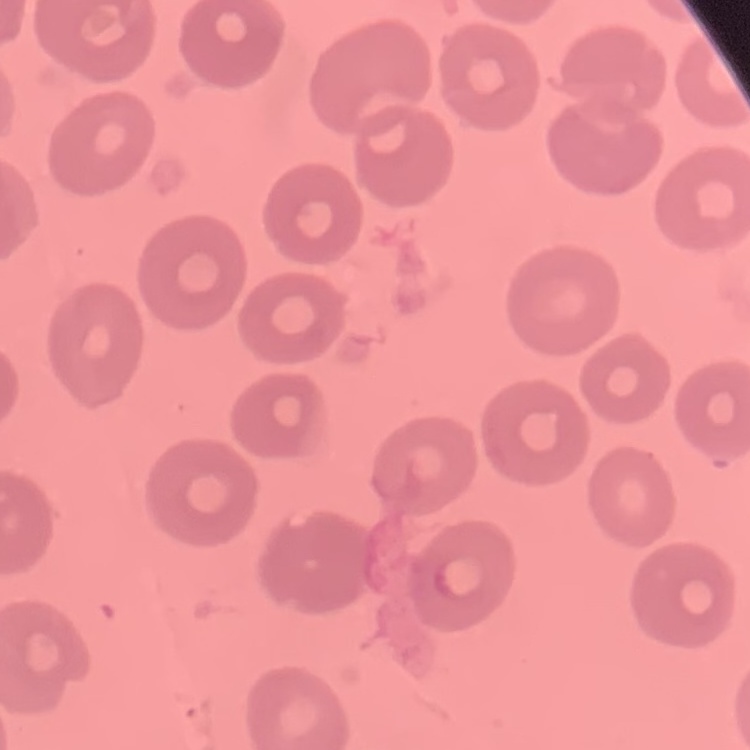
The red blood cells exhibit no rouleaux formation. Thin peripheral smear. Square crop of a larger photomicrograph. Field's or Giemsa stain.